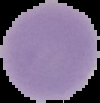
Summary:
  - Image size: 100×103 pixels
  - Malaria status: uninfected
  - Image type: segmented cell region with the area outside set to black
  - Preparation: thin blood film